Identify the blood parasite species.
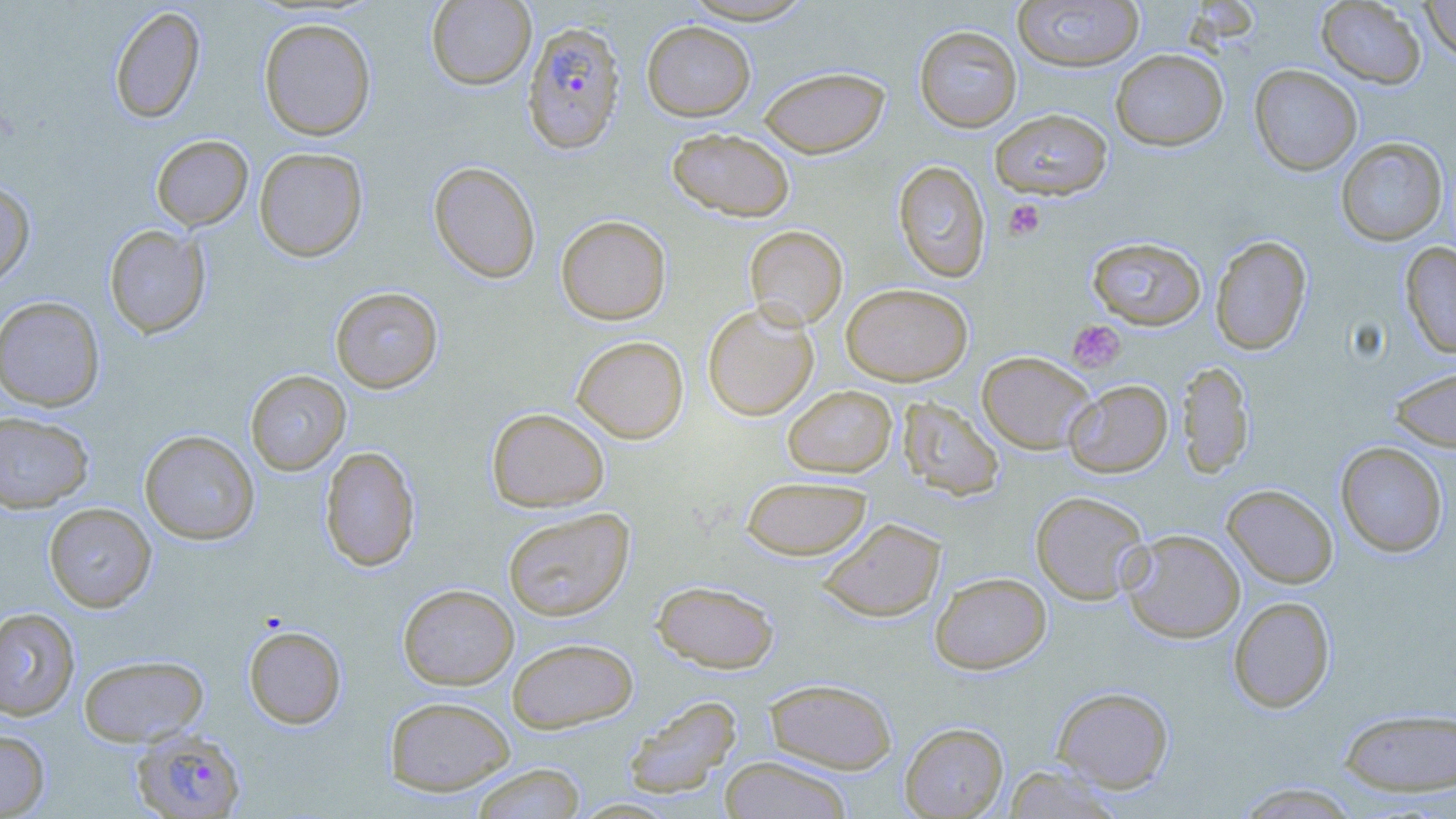
Plasmodium falciparum.

{
  "platelet_locations": "approximate bounding boxes as [x1, y1, x2, y2] in pixels: [1002, 199, 1045, 241], [1066, 319, 1126, 373]",
  "uninfected_red_blood_cell_locations": "approximate bounding boxes as [x1, y1, x2, y2] in pixels: [678, 0, 820, 25], [1011, 0, 1145, 72], [1420, 0, 1456, 63], [426, 1, 536, 90], [1316, 1, 1426, 89], [108, 6, 205, 125], [258, 16, 376, 141], [641, 20, 756, 121], [914, 25, 1022, 132], [1110, 49, 1229, 151], [1249, 65, 1362, 175], [759, 66, 889, 158], [989, 108, 1113, 200], [667, 128, 795, 221], [151, 135, 253, 231], [1335, 137, 1448, 246], [254, 147, 368, 262], [428, 161, 541, 284], [893, 161, 990, 283], [0, 179, 36, 289], [556, 215, 671, 325], [104, 224, 210, 339], [744, 225, 847, 330], [1210, 235, 1312, 355], [1086, 236, 1206, 330], [1401, 242, 1456, 358], [841, 283, 973, 385], [330, 286, 443, 393], [0, 296, 105, 412], [702, 303, 818, 421], [571, 336, 689, 443], [977, 351, 1096, 454], [1177, 360, 1255, 478], [1389, 366, 1456, 452], [245, 370, 350, 475], [1063, 379, 1173, 477], [782, 385, 897, 477], [897, 396, 1005, 501], [487, 407, 610, 512], [0, 411, 94, 513], [139, 430, 260, 545], [1335, 441, 1449, 557], [319, 446, 421, 572], [741, 475, 872, 560], [1222, 484, 1338, 588], [1030, 490, 1150, 604], [43, 502, 156, 612], [502, 508, 635, 621], [817, 517, 946, 622], [1121, 529, 1245, 643], [930, 572, 1052, 674], [652, 580, 779, 673], [398, 584, 519, 689], [1228, 596, 1335, 713], [0, 607, 80, 720], [243, 624, 347, 729], [507, 637, 638, 733], [79, 654, 208, 747], [764, 678, 898, 774], [1052, 686, 1174, 792], [384, 695, 516, 795], [624, 695, 742, 798], [1338, 707, 1456, 797], [899, 722, 1008, 818], [0, 730, 50, 817], [719, 756, 853, 818], [470, 763, 586, 819], [1002, 765, 1125, 818], [1233, 782, 1363, 818]",
  "plasmodium_falciparum_infected_red_blood_cell_locations": "approximate bounding boxes as [x1, y1, x2, y2] in pixels: [521, 20, 626, 154], [131, 729, 247, 818]",
  "image_size": "1456×819 pixels",
  "modality": "optical microscopy",
  "preparation": "thin blood film",
  "magnification": "1000x",
  "field_of_view": "one of a larger specimen",
  "stain": "May-Grünwald-Giemsa"
}